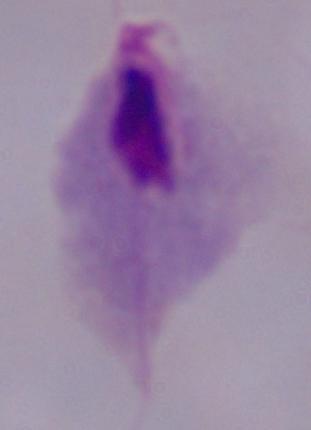

{
  "magnification": "1000x",
  "identification": "trichomonad",
  "modality": "photomicrograph"
}